Describe the morphology of the red blood cells.
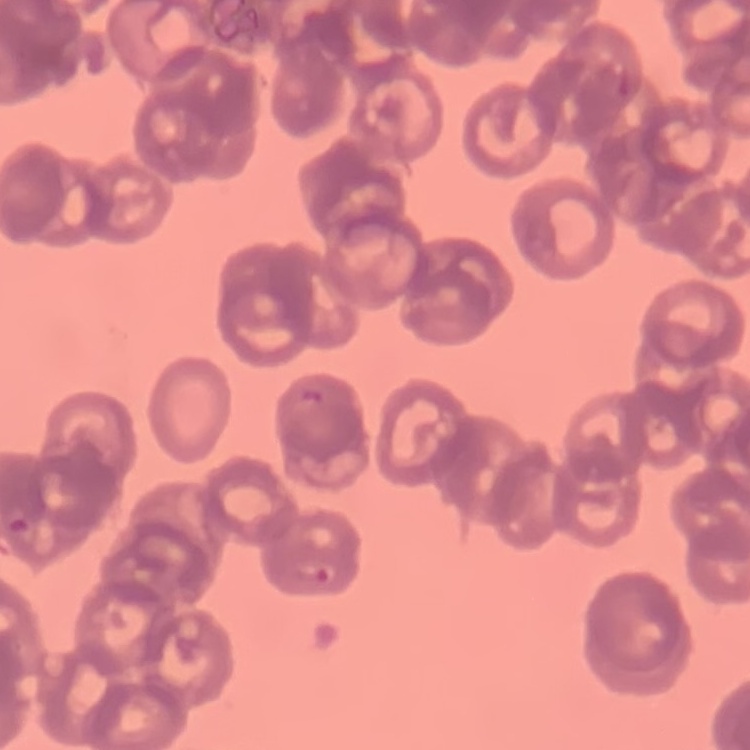

Rouleaux formation.

Summary:
  - Image type: square crop of a larger photomicrograph
  - Stain: Field's or Giemsa
  - Preparation: thin blood film